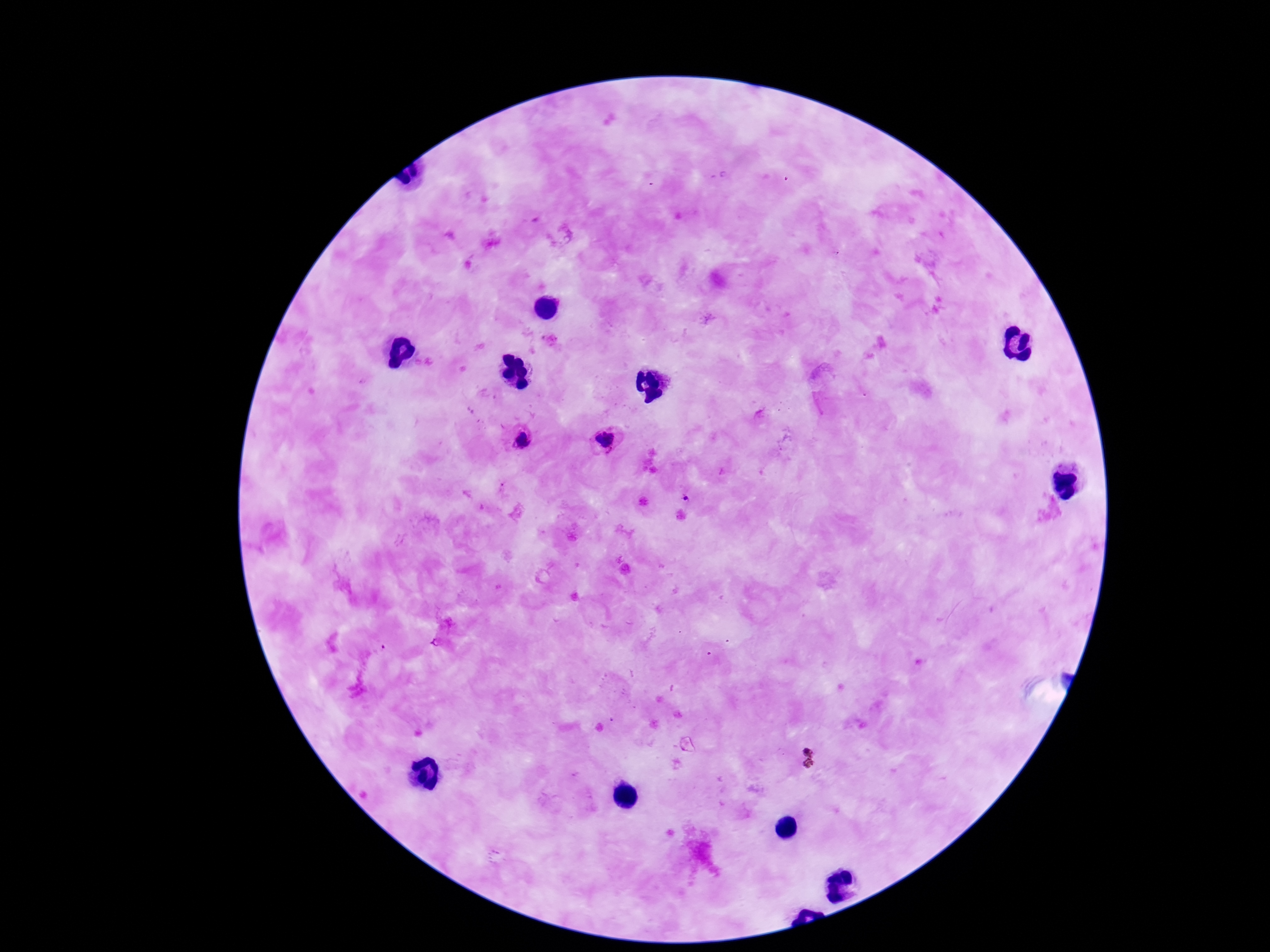
stain: Giemsa
image_size: 1270×952 pixels
capture: smartphone camera through the microscope eyepiece
magnification: 100x
field_of_view: one from this slide
preparation: thick blood smear
patient_malaria_status: positive
plasmodium_parasite_locations: 'approximate centers as {x, y} in pixels: {523, 442}, {605, 442}, {686, 497}'